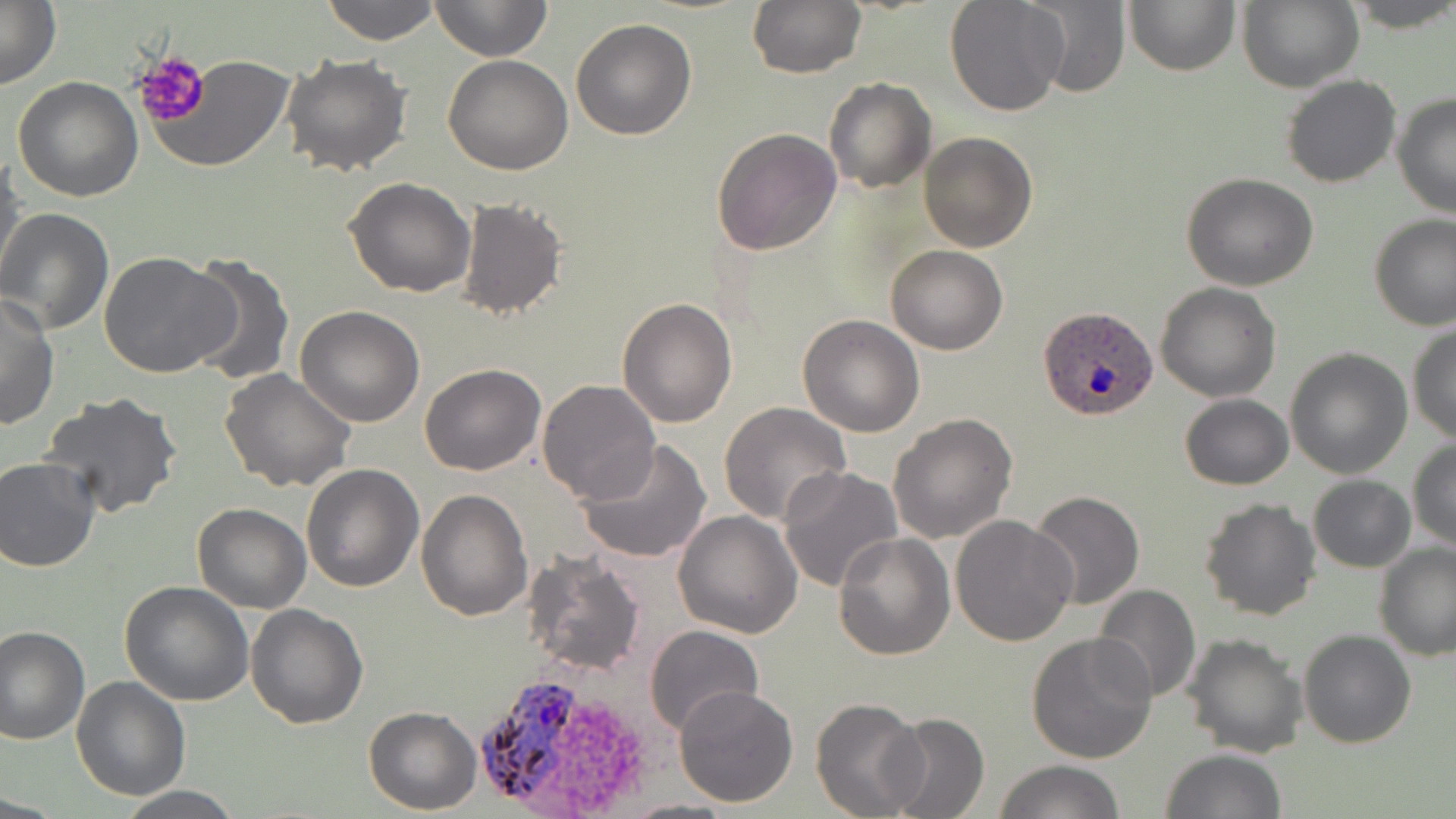
{
  "plasmodium_ovale_infected_red_blood_cell_locations": "approximate bounding boxes as (x1, y1, x2, y2) in pixels: (1037, 309, 1160, 423), (464, 665, 588, 816)",
  "slide_level_diagnosis": "Plasmodium ovale",
  "platelet_locations": "approximate bounding boxes as (x1, y1, x2, y2) in pixels: (133, 52, 212, 127)",
  "magnification": "1000x",
  "uninfected_red_blood_cell_locations": "approximate bounding boxes as (x1, y1, x2, y2) in pixels: (0, 0, 60, 91), (320, 0, 439, 45), (429, 0, 551, 62), (1017, 0, 1131, 97), (1123, 0, 1240, 75), (1237, 0, 1364, 93), (1345, 0, 1456, 32), (747, 1, 865, 78), (944, 1, 1070, 116), (569, 18, 697, 140), (280, 51, 413, 175), (147, 54, 295, 174), (442, 55, 573, 175), (1281, 75, 1401, 189), (12, 76, 143, 204), (824, 77, 936, 194), (1392, 91, 1456, 220), (711, 127, 842, 256), (917, 131, 1038, 253), (1, 152, 25, 285), (1181, 173, 1320, 292), (343, 177, 476, 297), (458, 196, 569, 321), (0, 208, 117, 335), (1369, 213, 1456, 331), (884, 244, 1008, 355), (98, 249, 237, 379), (179, 256, 294, 385), (1155, 282, 1281, 402), (0, 294, 59, 430), (617, 297, 739, 428), (294, 307, 425, 428), (797, 314, 925, 438), (1408, 324, 1455, 447), (1284, 347, 1413, 479), (419, 363, 546, 476), (219, 369, 356, 494), (535, 378, 661, 505), (38, 392, 183, 519), (1179, 394, 1293, 490), (719, 402, 851, 525), (889, 412, 1018, 543), (577, 438, 714, 565), (1408, 438, 1456, 552), (0, 458, 100, 572), (299, 463, 424, 592), (777, 465, 904, 593), (1308, 475, 1415, 572), (417, 488, 532, 621), (1027, 490, 1145, 609), (1198, 498, 1323, 621), (191, 502, 312, 613), (674, 511, 802, 639), (950, 515, 1078, 647), (833, 531, 957, 661), (1373, 542, 1456, 661), (523, 551, 646, 676), (120, 581, 253, 704), (1093, 583, 1201, 703), (246, 603, 368, 728), (643, 624, 765, 738), (1, 626, 91, 745), (1298, 630, 1415, 748), (1025, 631, 1158, 763), (1183, 633, 1308, 757), (72, 676, 190, 801), (673, 684, 799, 808), (810, 697, 928, 819), (363, 706, 483, 815), (883, 713, 988, 819), (1160, 748, 1287, 819), (993, 759, 1126, 818), (115, 785, 246, 818), (615, 796, 744, 818)",
  "stain": "May-Grünwald-Giemsa",
  "field_of_view": "single",
  "preparation": "thin blood smear",
  "modality": "light microscopy",
  "image_size": "1456×819 pixels"
}